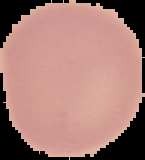
malaria status = uninfected
image size = 145×160 pixels
preparation = thin blood film
image type = segmented cell region on a black background